Point out each malaria parasite.
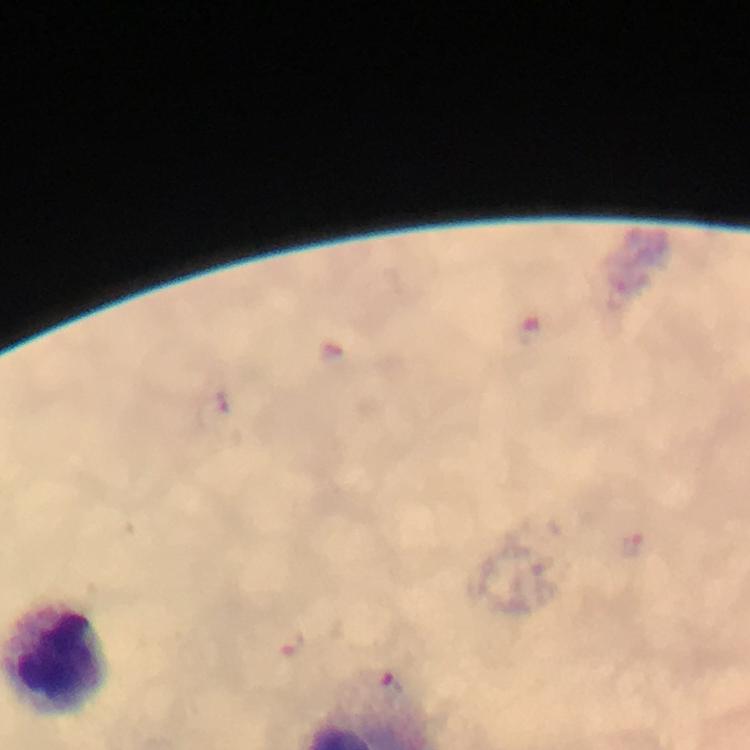
Approximate centers as (x, y) in pixels.
Malaria parasites: (217, 401), (633, 545), (290, 644), (390, 687).

stain = Giemsa
capture = smartphone mounted on the microscope
magnification = 100x
context = from a diagnostic examination for malaria
cropped from = one field of view
image size = 750×750 pixels
immersion oil = used
preparation = thick blood film